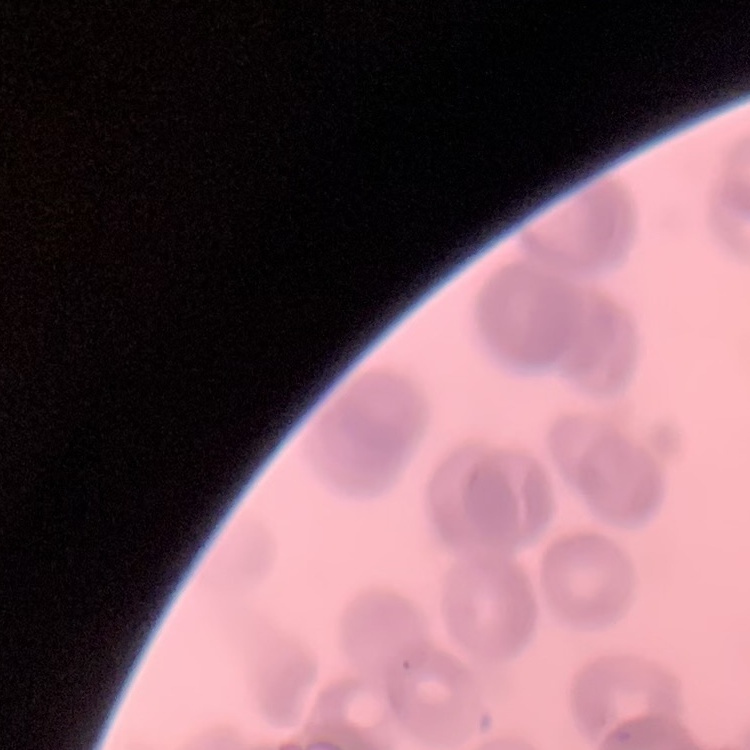
{
  "erythrocyte_morphology": "rouleaux formation",
  "image_type": "square crop of a larger photomicrograph",
  "stain": "Field's or Giemsa",
  "preparation": "thin blood film"
}